Name the cell type shown.
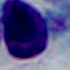
A leukocyte.

modality: photomicrograph
magnification: 1000x